Give the extent of all uninfected red blood cells.
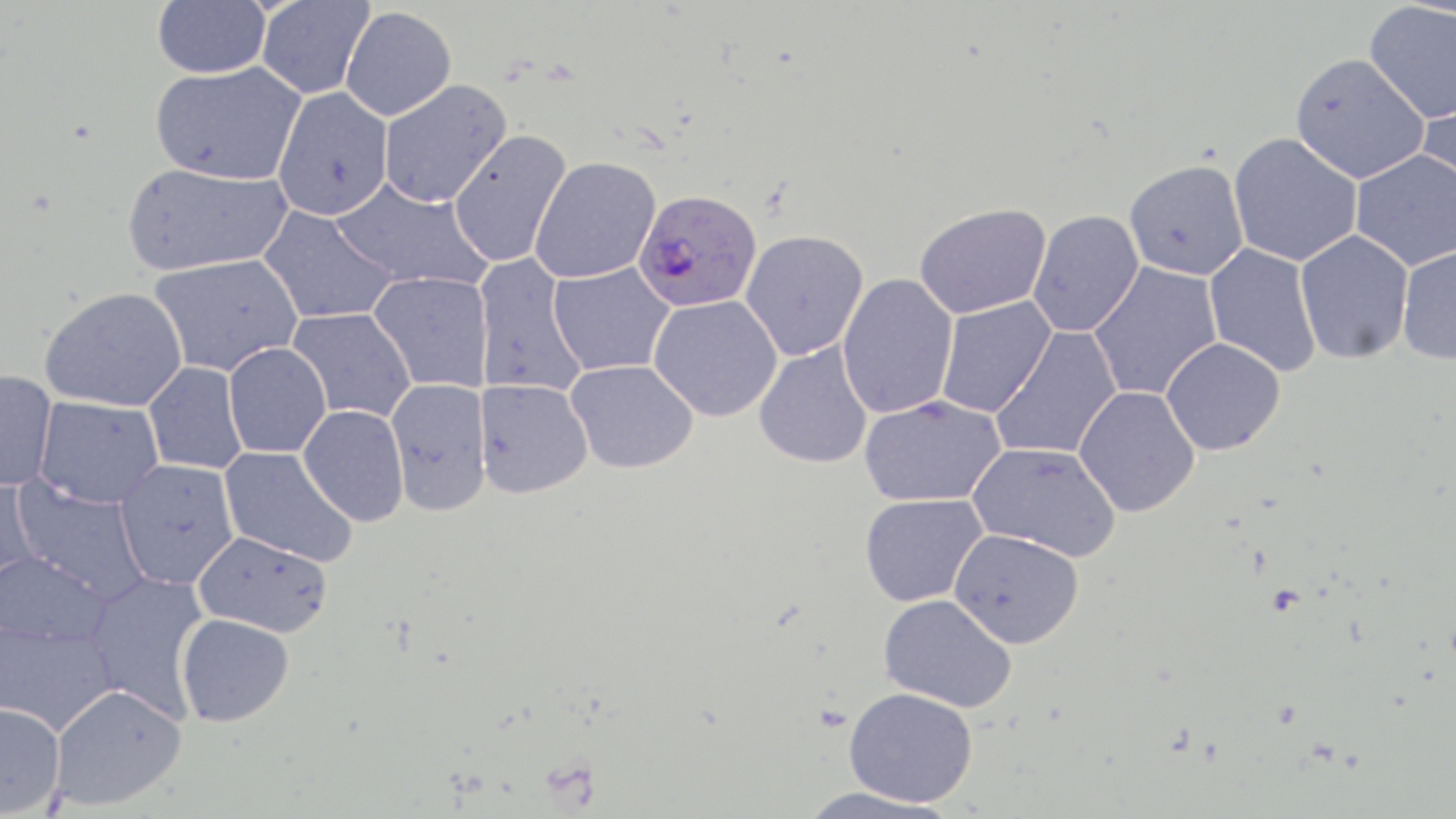
Approximate bounding boxes as (x1, y1, x2, y2) in pixels.
Uninfected red blood cells: (153, 0, 271, 78), (256, 1, 375, 99), (1363, 2, 1456, 124), (341, 7, 456, 121), (1290, 53, 1430, 184), (150, 61, 306, 186), (379, 79, 512, 208), (273, 87, 394, 221), (1418, 93, 1456, 213), (448, 129, 572, 268), (1228, 133, 1363, 266), (1350, 149, 1456, 271), (530, 156, 661, 284), (1124, 160, 1249, 280), (121, 162, 292, 275), (331, 176, 493, 293), (914, 203, 1051, 319), (259, 206, 398, 325), (1028, 210, 1144, 337), (740, 230, 869, 360), (1295, 230, 1414, 364), (1203, 244, 1322, 377), (1396, 245, 1456, 365), (148, 254, 302, 377), (474, 254, 588, 398), (1087, 261, 1224, 402), (548, 263, 675, 376), (368, 272, 492, 393), (837, 273, 958, 419), (39, 287, 188, 412), (648, 295, 783, 421), (934, 297, 1056, 419), (288, 308, 415, 423), (991, 326, 1122, 461), (1161, 338, 1286, 455), (224, 343, 331, 459), (754, 343, 873, 469), (566, 359, 698, 474), (144, 362, 249, 475), (0, 370, 57, 492), (387, 378, 491, 517), (474, 379, 594, 499), (1074, 386, 1200, 517), (857, 395, 1006, 507), (35, 396, 164, 508), (298, 405, 409, 526), (967, 442, 1121, 562), (219, 447, 357, 567), (114, 459, 239, 589), (0, 472, 43, 591), (8, 475, 151, 603), (859, 494, 988, 607), (949, 528, 1084, 648), (193, 531, 333, 636), (0, 550, 113, 646), (82, 570, 211, 720), (878, 594, 1016, 712), (176, 614, 293, 727), (0, 619, 117, 735), (50, 684, 186, 809), (843, 687, 978, 807), (0, 702, 65, 817), (795, 785, 960, 819).

Summary:
  - Plasmodium falciparum-infected red blood cell locations: (634, 189, 762, 313)
  - Slide-level diagnosis: Plasmodium falciparum
  - Magnification: 1000x
  - Modality: optical microscopy
  - Stain: May-Grünwald-Giemsa
  - Image size: 1456×819 pixels
  - Field of view: one of a larger specimen
  - Preparation: thin blood smear